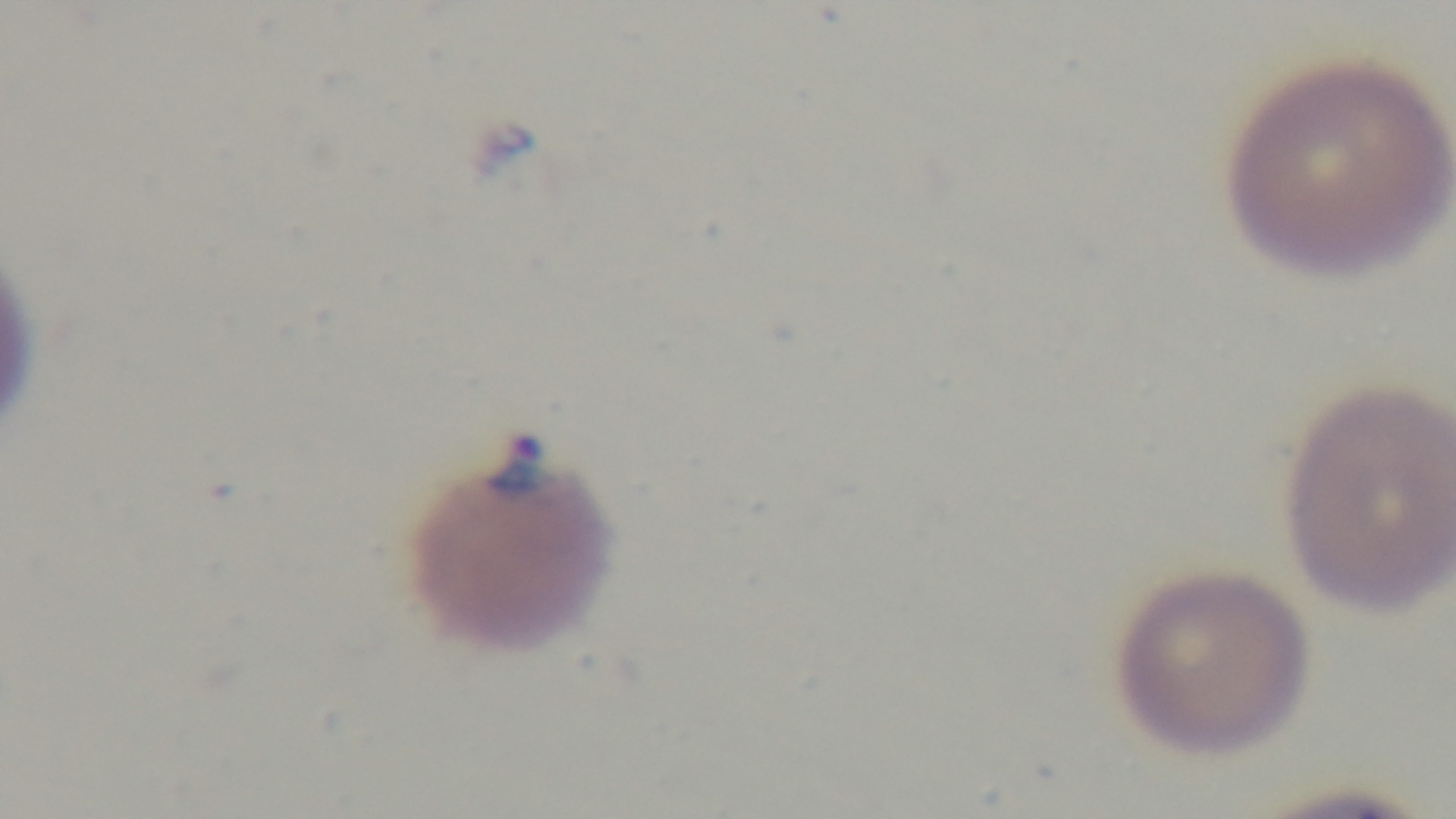

Captured with a mounted 4K digital camera. Giemsa-stained. Single field of view. Malaria status: positive. Preparation: thin. Oil-immersion objective, 100x. Photomicrograph.